Name the cell type shown.
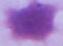

This is an erythrocyte.

1000x magnification. Micrograph.